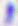
Summary:
  - Identification: Toxoplasma gondii
  - Modality: micrograph
  - Magnification: 400x